Assess this cell for malaria.
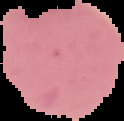
Uninfected.

image type = segmented cell region on a black background
image size = 124×121 pixels
preparation = thin blood smear